Comment on the morphology of the erythrocytes.
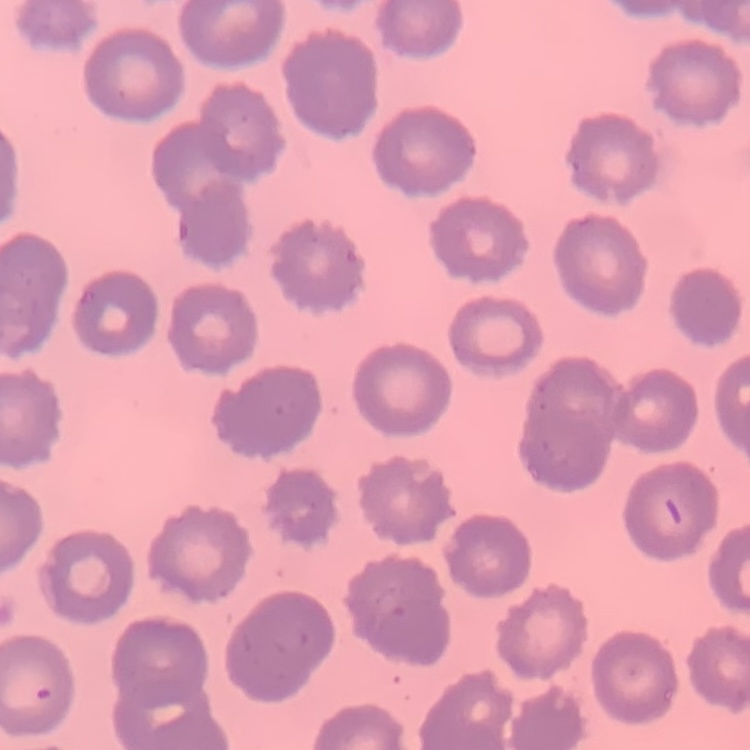

No rouleaux formation.

image type = square crop of a larger photomicrograph
preparation = thin peripheral smear
stain = Field's or Giemsa